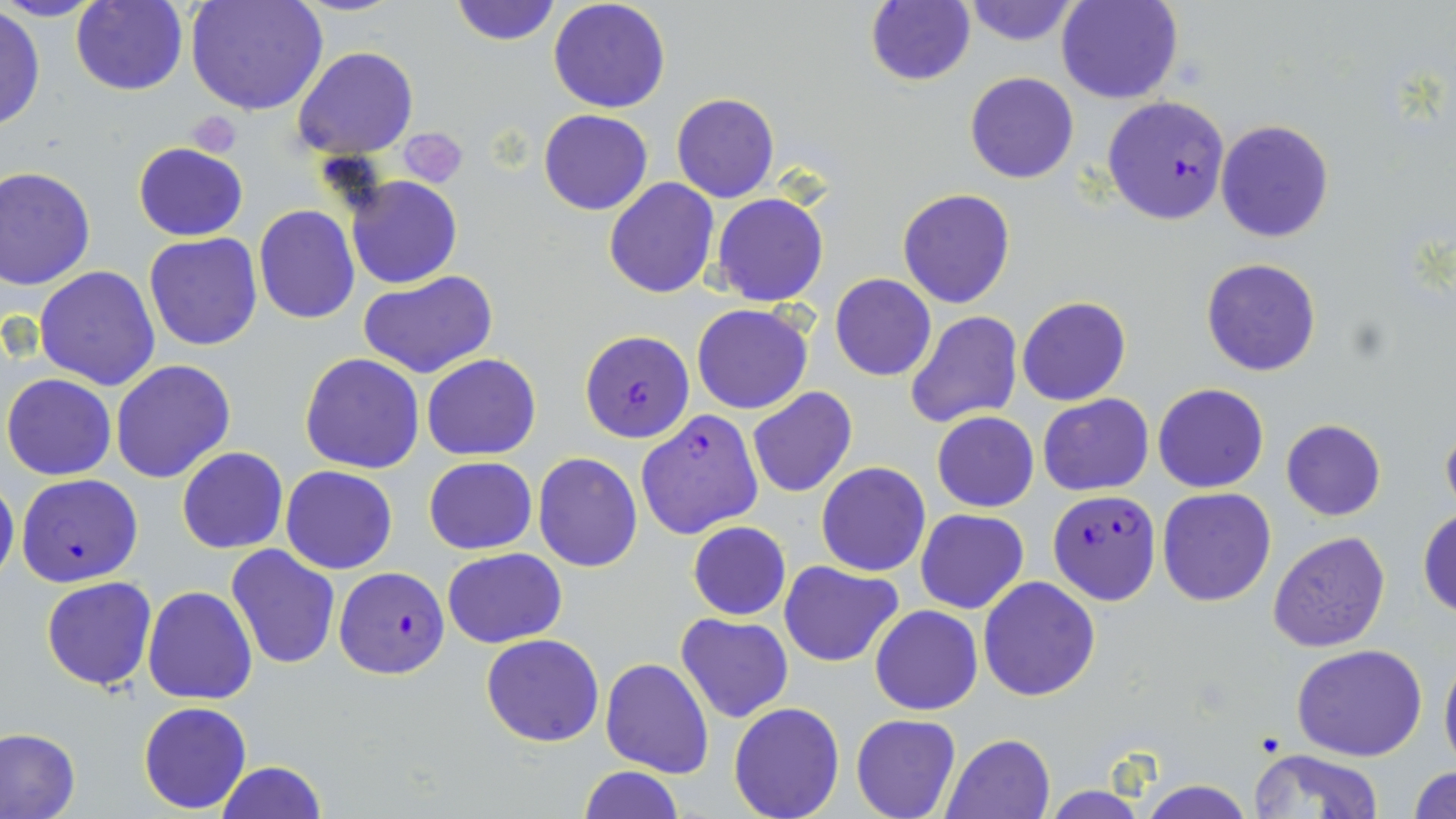
slide-level diagnosis = Plasmodium falciparum
field of view = one of a larger specimen
image size = 1456×819 pixels
preparation = thin blood film
platelet locations = approximate bounding boxes as named x1/y1/x2/y2 corners in pixels: (x1=188, y1=112, x2=242, y2=157), (x1=397, y1=128, x2=468, y2=189)
modality = light microscopy
stain = May-Grünwald-Giemsa
uninfected red blood cell locations = approximate bounding boxes as named x1/y1/x2/y2 corners in pixels: (x1=4, y1=0, x2=106, y2=22), (x1=69, y1=0, x2=188, y2=94), (x1=185, y1=0, x2=326, y2=117), (x1=450, y1=0, x2=560, y2=45), (x1=548, y1=0, x2=672, y2=114), (x1=960, y1=0, x2=1081, y2=46), (x1=1056, y1=0, x2=1184, y2=105), (x1=865, y1=1, x2=975, y2=86), (x1=1, y1=6, x2=45, y2=132), (x1=294, y1=46, x2=418, y2=159), (x1=965, y1=73, x2=1078, y2=184), (x1=672, y1=94, x2=780, y2=203), (x1=539, y1=109, x2=653, y2=215), (x1=1216, y1=120, x2=1334, y2=243), (x1=132, y1=142, x2=248, y2=241), (x1=0, y1=166, x2=96, y2=289), (x1=347, y1=175, x2=461, y2=289), (x1=604, y1=176, x2=718, y2=297), (x1=897, y1=188, x2=1016, y2=309), (x1=713, y1=193, x2=827, y2=306), (x1=253, y1=204, x2=360, y2=323), (x1=144, y1=232, x2=265, y2=351), (x1=1201, y1=259, x2=1321, y2=377), (x1=35, y1=266, x2=162, y2=391), (x1=358, y1=270, x2=498, y2=380), (x1=830, y1=273, x2=937, y2=381), (x1=1016, y1=296, x2=1131, y2=406), (x1=692, y1=303, x2=814, y2=414), (x1=904, y1=312, x2=1023, y2=429), (x1=299, y1=353, x2=425, y2=474), (x1=422, y1=354, x2=542, y2=459), (x1=112, y1=359, x2=235, y2=484), (x1=2, y1=373, x2=116, y2=481), (x1=1154, y1=383, x2=1268, y2=493), (x1=746, y1=386, x2=858, y2=498), (x1=1038, y1=393, x2=1154, y2=495), (x1=635, y1=409, x2=764, y2=539), (x1=931, y1=410, x2=1039, y2=512), (x1=1440, y1=413, x2=1456, y2=522), (x1=1280, y1=419, x2=1386, y2=521), (x1=177, y1=447, x2=287, y2=554), (x1=534, y1=452, x2=643, y2=572), (x1=424, y1=456, x2=537, y2=554), (x1=816, y1=462, x2=932, y2=575), (x1=281, y1=465, x2=398, y2=574), (x1=0, y1=477, x2=19, y2=589), (x1=1158, y1=488, x2=1275, y2=607), (x1=1418, y1=507, x2=1456, y2=620), (x1=915, y1=508, x2=1029, y2=613), (x1=687, y1=522, x2=792, y2=620), (x1=1268, y1=531, x2=1390, y2=652), (x1=225, y1=544, x2=340, y2=668), (x1=441, y1=547, x2=567, y2=647), (x1=780, y1=560, x2=904, y2=668), (x1=978, y1=576, x2=1102, y2=701), (x1=42, y1=577, x2=158, y2=691), (x1=142, y1=585, x2=258, y2=706), (x1=869, y1=605, x2=982, y2=715), (x1=676, y1=612, x2=793, y2=723), (x1=480, y1=633, x2=604, y2=747), (x1=1291, y1=644, x2=1429, y2=761), (x1=1439, y1=646, x2=1456, y2=775), (x1=600, y1=658, x2=714, y2=778), (x1=137, y1=701, x2=252, y2=813), (x1=728, y1=701, x2=845, y2=819), (x1=851, y1=714, x2=960, y2=819), (x1=1, y1=728, x2=80, y2=819), (x1=942, y1=732, x2=1055, y2=818), (x1=1248, y1=748, x2=1384, y2=819), (x1=215, y1=760, x2=326, y2=819), (x1=576, y1=765, x2=685, y2=819), (x1=1408, y1=765, x2=1456, y2=818), (x1=1134, y1=777, x2=1255, y2=818), (x1=1042, y1=784, x2=1150, y2=819)
magnification = 1000x
Plasmodium falciparum-infected red blood cell locations = approximate bounding boxes as named x1/y1/x2/y2 corners in pixels: (x1=1102, y1=96, x2=1231, y2=225), (x1=580, y1=328, x2=695, y2=442), (x1=16, y1=473, x2=143, y2=587), (x1=1046, y1=489, x2=1161, y2=605), (x1=334, y1=566, x2=451, y2=680)